Point out each Plasmodium parasite.
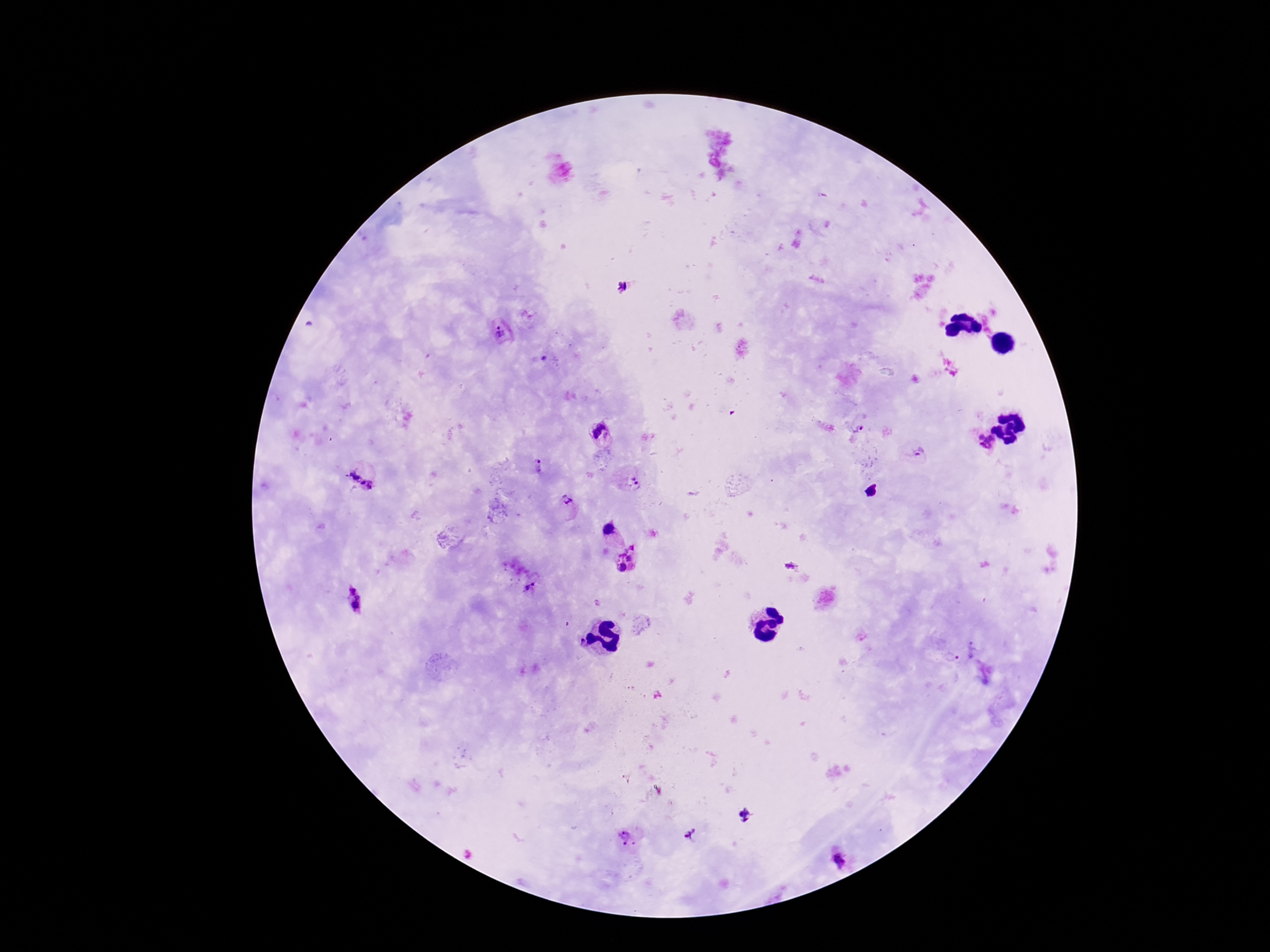
Approximate object centers, in pixels from the top-left corner.
Plasmodium parasites: (x=621, y=287), (x=501, y=332), (x=856, y=430), (x=599, y=433), (x=985, y=442), (x=917, y=453), (x=539, y=465), (x=362, y=477), (x=632, y=478), (x=636, y=483), (x=566, y=499), (x=608, y=529), (x=632, y=547), (x=629, y=558), (x=792, y=566), (x=621, y=567), (x=534, y=584), (x=527, y=587), (x=354, y=600), (x=581, y=642), (x=952, y=657), (x=746, y=815), (x=689, y=834), (x=627, y=838), (x=840, y=860).

{
  "preparation": "thick blood smear",
  "patient_malaria_status": "infected",
  "magnification": "100x",
  "image_size": "1270×952 pixels",
  "stain": "Giemsa",
  "field_of_view": "one from this slide",
  "capture": "smartphone camera through the microscope eyepiece"
}